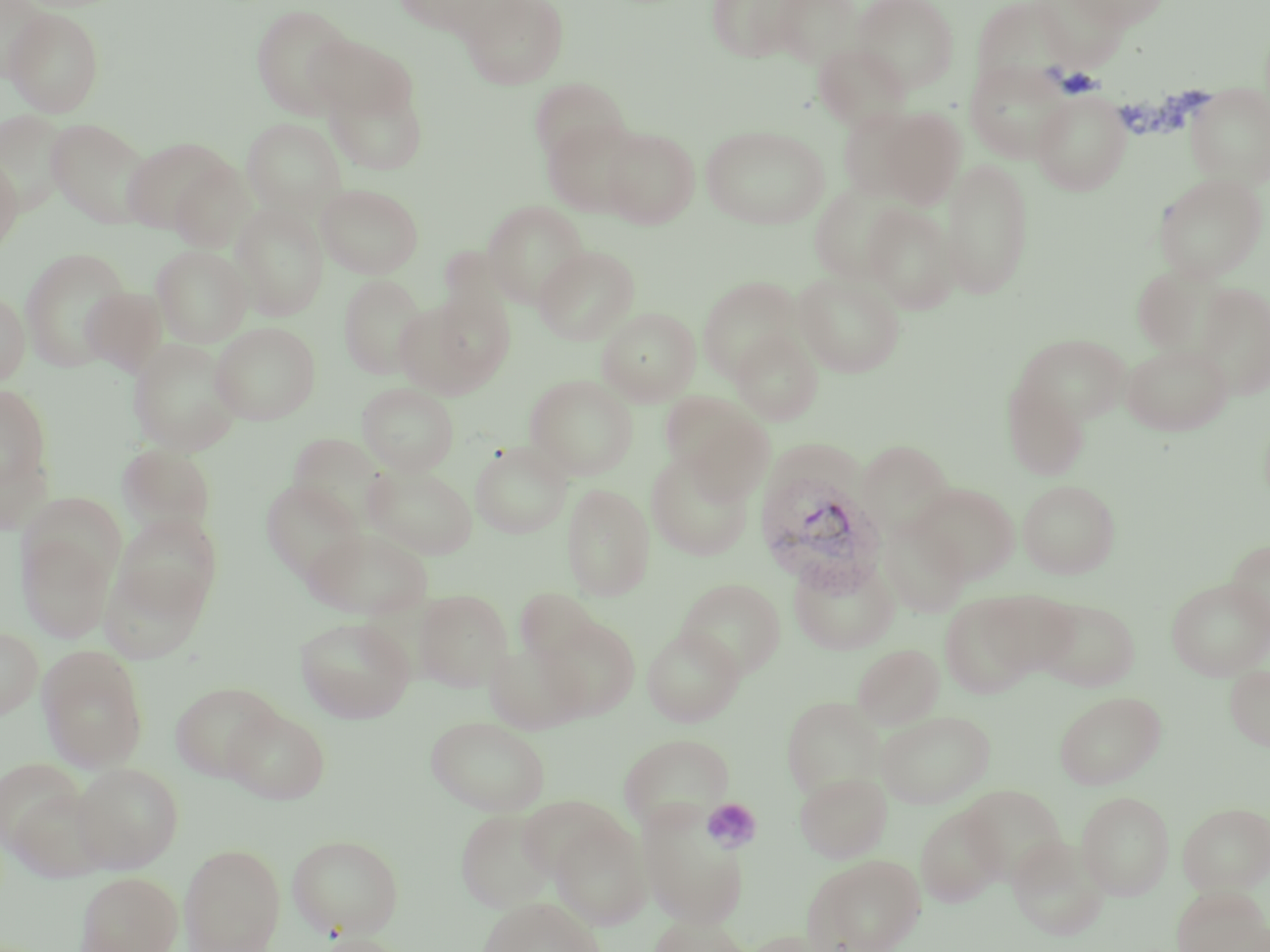

{
  "slide_level_diagnosis": "Plasmodium vivax",
  "image_size": "1270×952 pixels",
  "plasmodium_vivax_infected_red_blood_cell_locations": "approximate bounding boxes as (x1,y1)-(x2,y2) corner pairs in pixels: (755,470)-(886,593)",
  "modality": "optical microscopy",
  "field_of_view": "single",
  "preparation": "thin blood smear",
  "uninfected_red_blood_cell_locations": "approximate bounding boxes as (x1,y1)-(x2,y2) corner pairs in pixels: (391,0)-(504,36), (462,0)-(569,89), (706,0)-(807,62), (771,0)-(863,68), (852,0)-(959,94), (972,0)-(1069,89), (1034,0)-(1128,70), (1066,0)-(1171,29), (1,1)-(53,82), (250,4)-(357,117), (4,7)-(105,118), (308,34)-(416,123), (813,42)-(911,132), (965,61)-(1071,163), (324,76)-(428,175), (529,77)-(630,166), (1185,83)-(1270,189), (1032,90)-(1131,195), (872,108)-(966,209), (0,109)-(72,214), (242,118)-(346,217), (47,119)-(151,227), (542,119)-(643,217), (701,125)-(830,229), (601,127)-(700,228), (121,136)-(238,237), (0,154)-(23,256), (941,157)-(1034,300), (1154,173)-(1268,282), (808,182)-(909,285), (316,184)-(423,278), (231,201)-(329,320), (482,201)-(589,309), (863,203)-(960,314), (151,244)-(252,347), (534,245)-(640,345), (19,246)-(133,373), (1132,264)-(1237,360), (793,272)-(905,378), (338,275)-(428,379), (698,276)-(803,382), (1194,283)-(1270,400), (81,286)-(168,377), (409,287)-(514,391), (0,289)-(31,388), (597,307)-(700,405), (210,322)-(320,425), (731,330)-(823,425), (1013,333)-(1130,426), (128,338)-(243,455), (1122,343)-(1232,435), (525,374)-(638,479), (1007,381)-(1099,576), (357,382)-(459,476), (1003,382)-(1090,480), (0,385)-(53,493), (663,394)-(771,493), (287,432)-(391,528), (856,440)-(955,538), (470,441)-(573,539), (117,444)-(216,537), (0,447)-(54,536), (645,452)-(753,560), (364,465)-(478,560), (1017,479)-(1120,578), (260,480)-(365,583), (562,483)-(655,600), (912,483)-(1020,584), (112,512)-(223,620), (879,519)-(971,618), (304,526)-(432,620), (18,529)-(116,643), (1226,539)-(1270,641), (788,555)-(899,655), (100,558)-(209,664), (676,578)-(785,679), (1168,578)-(1269,680), (514,588)-(601,669), (414,589)-(513,692), (985,590)-(1081,679), (940,594)-(1040,699), (1034,598)-(1139,691), (295,615)-(416,723), (540,615)-(640,720), (0,626)-(43,719), (642,626)-(743,727), (485,641)-(586,735), (852,643)-(945,729), (37,645)-(149,771), (1225,665)-(1270,750), (170,681)-(282,782), (1054,691)-(1166,790), (781,696)-(885,799), (223,705)-(330,804), (876,710)-(995,808), (425,716)-(550,815), (619,733)-(734,832), (0,757)-(91,861), (71,763)-(184,873), (794,771)-(892,862), (960,784)-(1067,883), (1076,791)-(1174,900), (1178,801)-(1270,894), (915,805)-(1006,908), (637,806)-(749,929), (455,808)-(559,912), (548,816)-(653,931), (287,834)-(404,939), (1007,835)-(1109,941), (179,844)-(286,952), (803,853)-(926,952), (75,871)-(183,952), (1171,885)-(1269,952), (477,896)-(605,952), (647,915)-(752,952), (738,929)-(843,952), (304,932)-(411,952)",
  "magnification": "1000x",
  "platelet_locations": "approximate bounding boxes as (x1,y1)-(x2,y2) corner pairs in pixels: (615,732)-(737,832), (702,798)-(762,852)",
  "stain": "May-Grünwald-Giemsa"
}